Assess the morphology of the red blood cells.
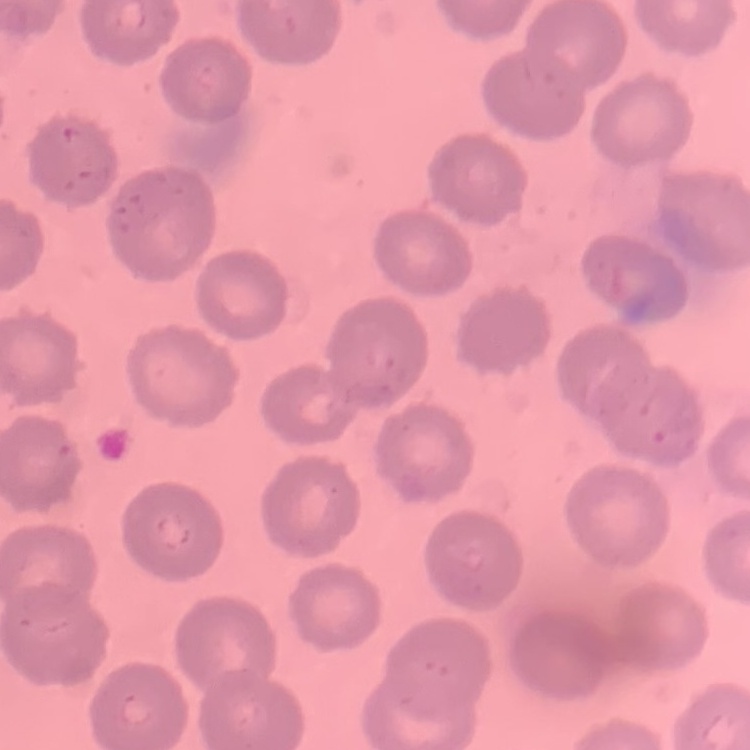

They show no rouleaux formation.

Summary:
  - Preparation: thin peripheral smear
  - Stain: Field's or Giemsa
  - Image type: square crop of a larger photomicrograph